Locate every blood parasite and identify its species.
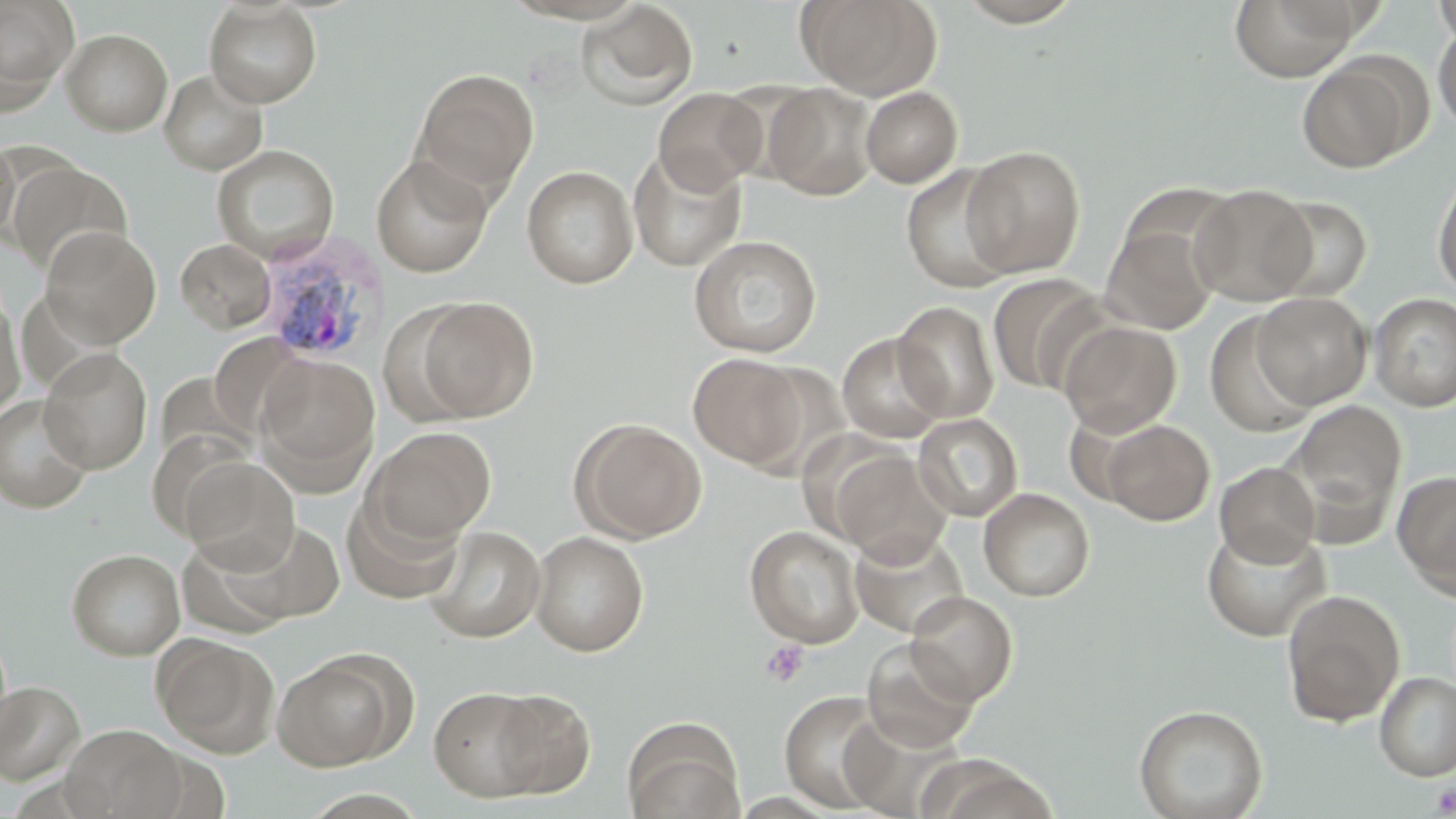
Approximate bounding boxes as named x1/y1/x2/y2 corners in pixels.
Plasmodium vivax-infected red blood cells: (x1=253, y1=231, x2=387, y2=366).
No Plasmodium falciparum, Plasmodium ovale, Plasmodium malariae, Babesia divergens, or Trypanosoma brucei observed.

Summary:
  - Platelet locations: (x1=759, y1=640, x2=809, y2=688), (x1=1431, y1=784, x2=1456, y2=817)
  - Uninfected red blood cell locations: (x1=0, y1=0, x2=78, y2=107), (x1=797, y1=0, x2=941, y2=99), (x1=953, y1=0, x2=1088, y2=27), (x1=1230, y1=0, x2=1360, y2=81), (x1=1432, y1=0, x2=1456, y2=47), (x1=577, y1=1, x2=699, y2=111), (x1=204, y1=2, x2=322, y2=108), (x1=1433, y1=22, x2=1456, y2=133), (x1=61, y1=28, x2=172, y2=136), (x1=1297, y1=56, x2=1420, y2=173), (x1=412, y1=68, x2=538, y2=197), (x1=159, y1=69, x2=268, y2=175), (x1=764, y1=83, x2=878, y2=201), (x1=860, y1=86, x2=963, y2=188), (x1=653, y1=88, x2=767, y2=195), (x1=0, y1=137, x2=19, y2=244), (x1=212, y1=144, x2=339, y2=263), (x1=961, y1=145, x2=1086, y2=278), (x1=628, y1=149, x2=746, y2=271), (x1=371, y1=155, x2=493, y2=277), (x1=7, y1=161, x2=131, y2=275), (x1=522, y1=164, x2=638, y2=289), (x1=901, y1=164, x2=1016, y2=292), (x1=1433, y1=170, x2=1456, y2=299), (x1=1190, y1=184, x2=1316, y2=305), (x1=1263, y1=195, x2=1373, y2=303), (x1=1101, y1=225, x2=1219, y2=334), (x1=40, y1=226, x2=161, y2=348), (x1=688, y1=234, x2=822, y2=357), (x1=176, y1=239, x2=276, y2=333), (x1=986, y1=272, x2=1108, y2=395), (x1=0, y1=291, x2=26, y2=417), (x1=1252, y1=292, x2=1372, y2=409), (x1=1369, y1=293, x2=1456, y2=411), (x1=412, y1=296, x2=539, y2=422), (x1=893, y1=300, x2=999, y2=424), (x1=379, y1=303, x2=485, y2=430), (x1=1205, y1=311, x2=1316, y2=437), (x1=1059, y1=321, x2=1182, y2=437), (x1=837, y1=332, x2=949, y2=444), (x1=209, y1=333, x2=310, y2=440), (x1=38, y1=348, x2=153, y2=474), (x1=255, y1=353, x2=380, y2=492), (x1=688, y1=353, x2=805, y2=468), (x1=0, y1=394, x2=94, y2=513), (x1=1286, y1=399, x2=1407, y2=542), (x1=913, y1=413, x2=1023, y2=522), (x1=575, y1=420, x2=706, y2=542), (x1=1101, y1=420, x2=1215, y2=525), (x1=365, y1=426, x2=497, y2=546), (x1=831, y1=448, x2=952, y2=566), (x1=180, y1=455, x2=299, y2=571), (x1=1214, y1=462, x2=1321, y2=566), (x1=1393, y1=470, x2=1456, y2=597), (x1=978, y1=487, x2=1095, y2=601), (x1=341, y1=490, x2=466, y2=604), (x1=192, y1=519, x2=347, y2=629), (x1=1201, y1=523, x2=1330, y2=641), (x1=425, y1=525, x2=546, y2=643), (x1=745, y1=525, x2=864, y2=648), (x1=530, y1=531, x2=649, y2=656), (x1=850, y1=531, x2=969, y2=638), (x1=67, y1=548, x2=185, y2=660), (x1=1281, y1=589, x2=1405, y2=727), (x1=905, y1=590, x2=1018, y2=706), (x1=153, y1=634, x2=279, y2=756), (x1=862, y1=642, x2=979, y2=753), (x1=273, y1=652, x2=405, y2=771), (x1=1374, y1=671, x2=1456, y2=782), (x1=0, y1=680, x2=85, y2=784), (x1=428, y1=686, x2=550, y2=801), (x1=489, y1=689, x2=595, y2=797), (x1=780, y1=691, x2=894, y2=812), (x1=1133, y1=703, x2=1268, y2=819), (x1=623, y1=720, x2=746, y2=819), (x1=61, y1=724, x2=187, y2=819)
  - Slide-level diagnosis: Plasmodium vivax
  - Magnification: 1000x
  - Modality: optical microscopy
  - Preparation: thin blood film
  - Field of view: single
  - Stain: May-Grünwald-Giemsa
  - Image size: 1456×819 pixels